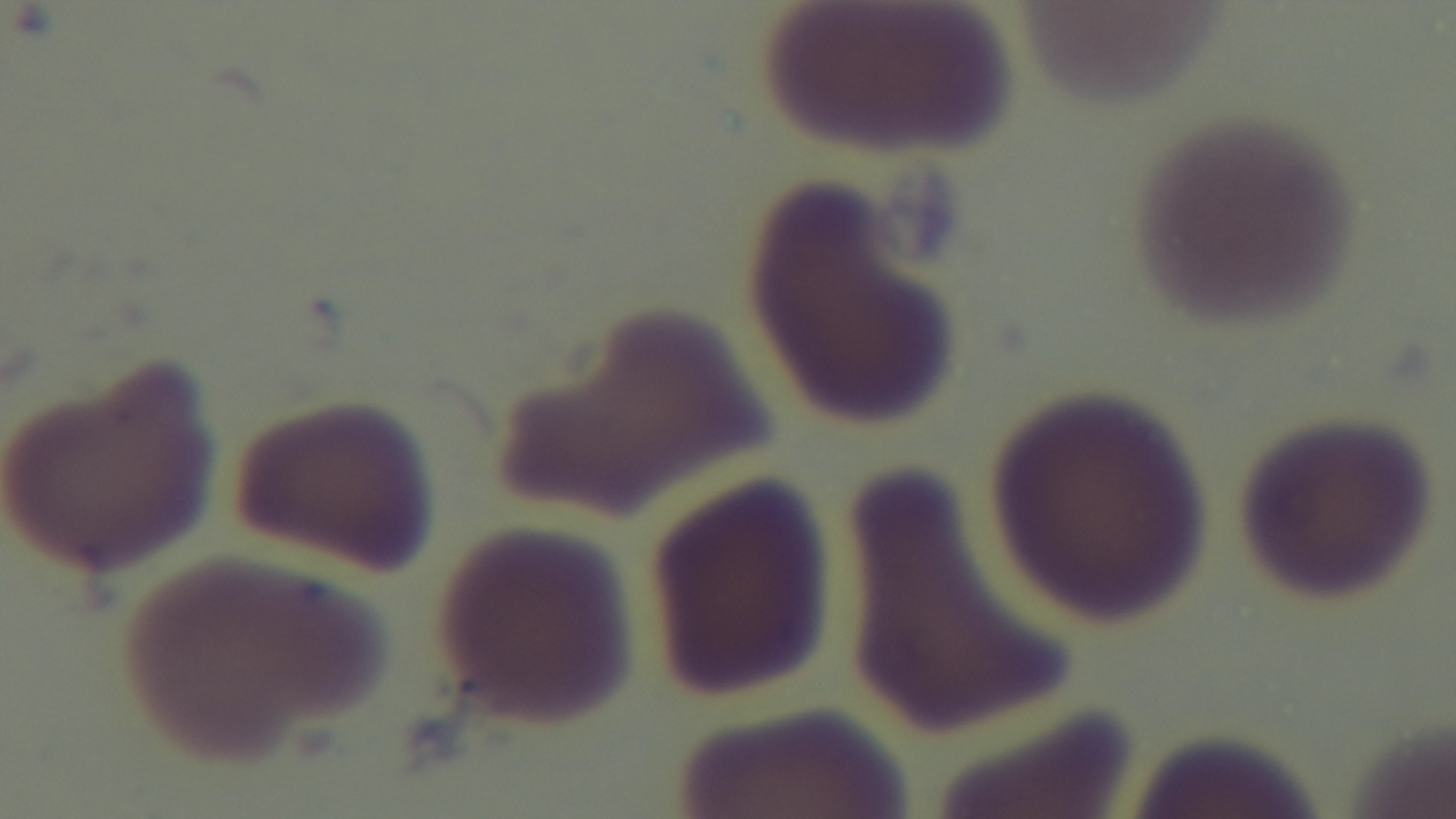
Summary:
  - Preparation: thin blood film
  - Capture: mounted 4K digital camera
  - Stain: Giemsa
  - Modality: light microscopy
  - Objective: 100x oil immersion
  - Field of view: single
  - Malaria status: uninfected